State which parasite is depicted.
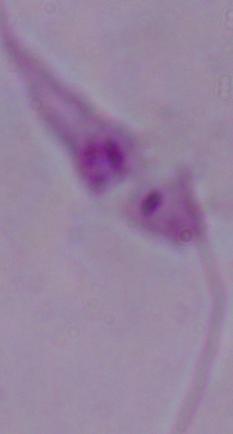

Leishmania.

Micrograph. 1000x magnification.